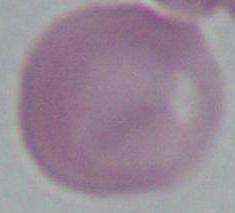

1000x magnification. A red blood cell is seen. Micrograph.